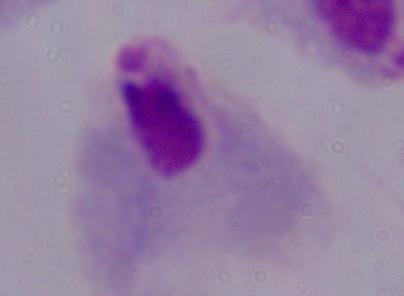
Summary:
  - Modality: micrograph
  - Identification: trichomonad
  - Magnification: 1000x